Point out each Plasmodium parasite.
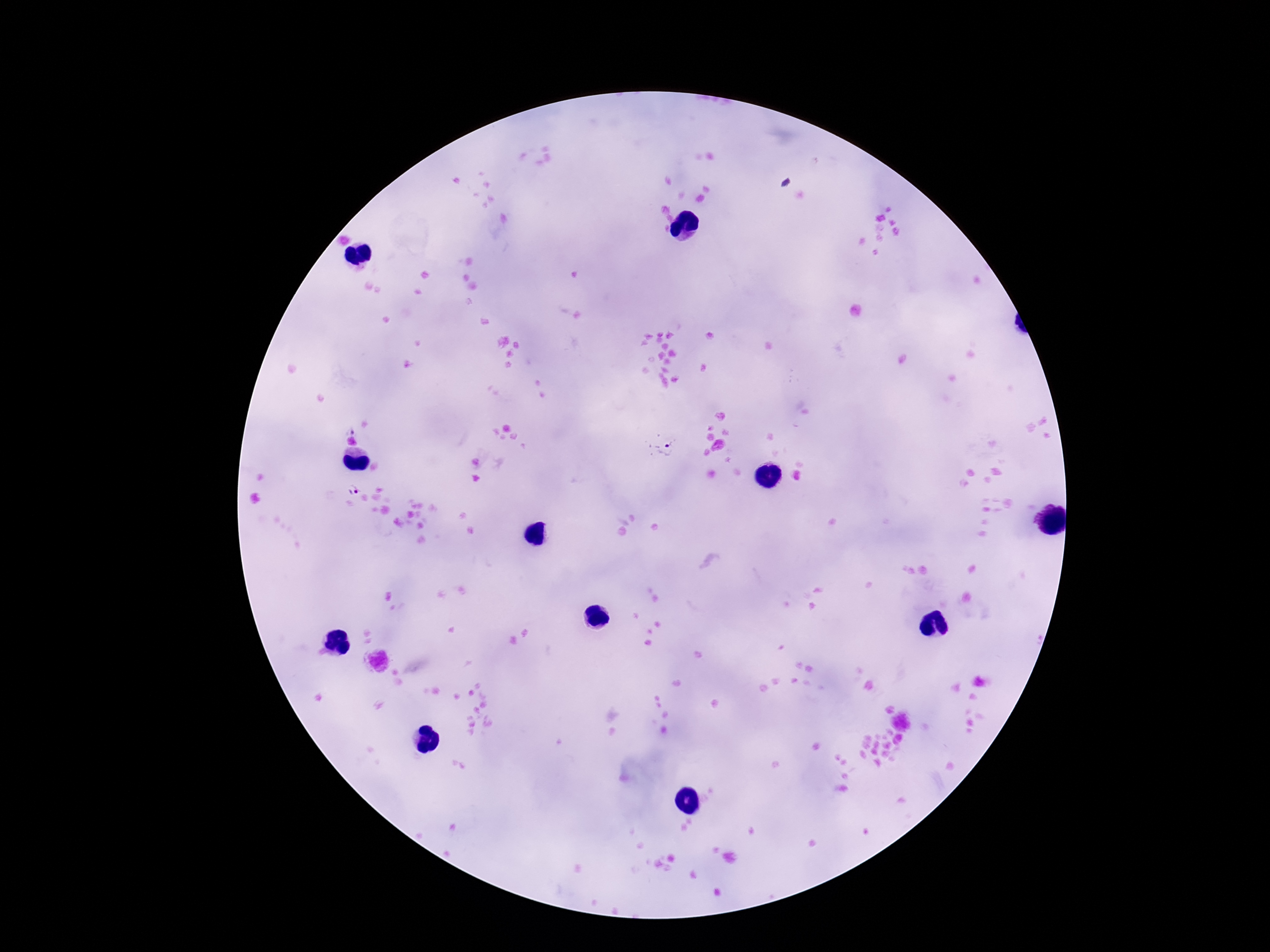
Approximate centers as (x, y) in pixels.
Plasmodium parasites: (350, 429), (671, 449), (352, 488).

Summary:
  - Magnification: 100x
  - Capture: smartphone camera through the microscope eyepiece
  - Patient malaria status: infected
  - Stain: Giemsa
  - Image size: 1270×952 pixels
  - Field of view: one from this slide
  - Preparation: thick blood film